Classify this cell by malaria status.
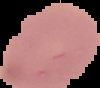
It is uninfected.

Cell region segmented out of the field of view; the surrounding area is masked to black. From a thin blood smear. Image is 100×88 pixels.